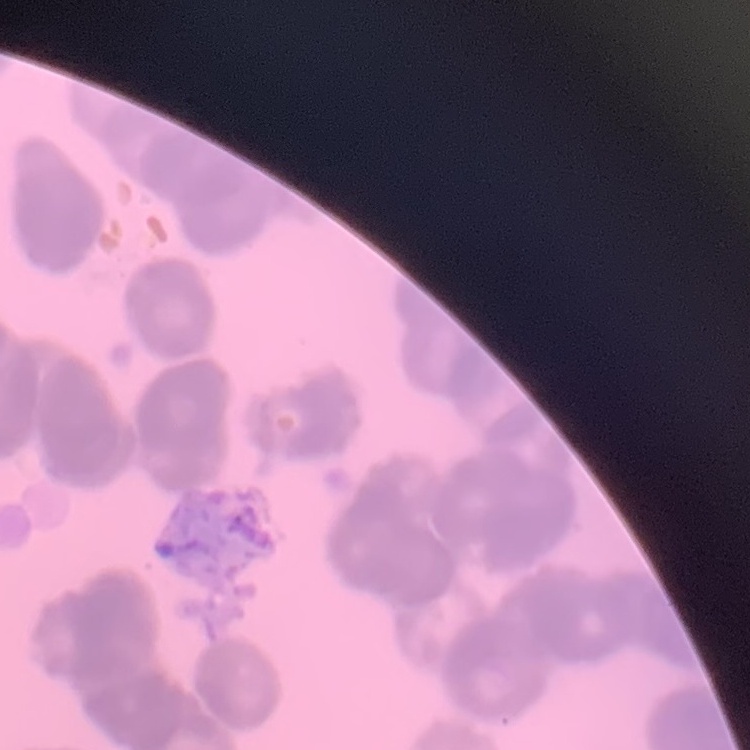

{
  "erythrocyte_morphology": "rouleaux formation",
  "stain": "Field's or Giemsa",
  "image_type": "one tile cut from a larger photomicrograph",
  "preparation": "thin peripheral smear"
}